Locate platelets.
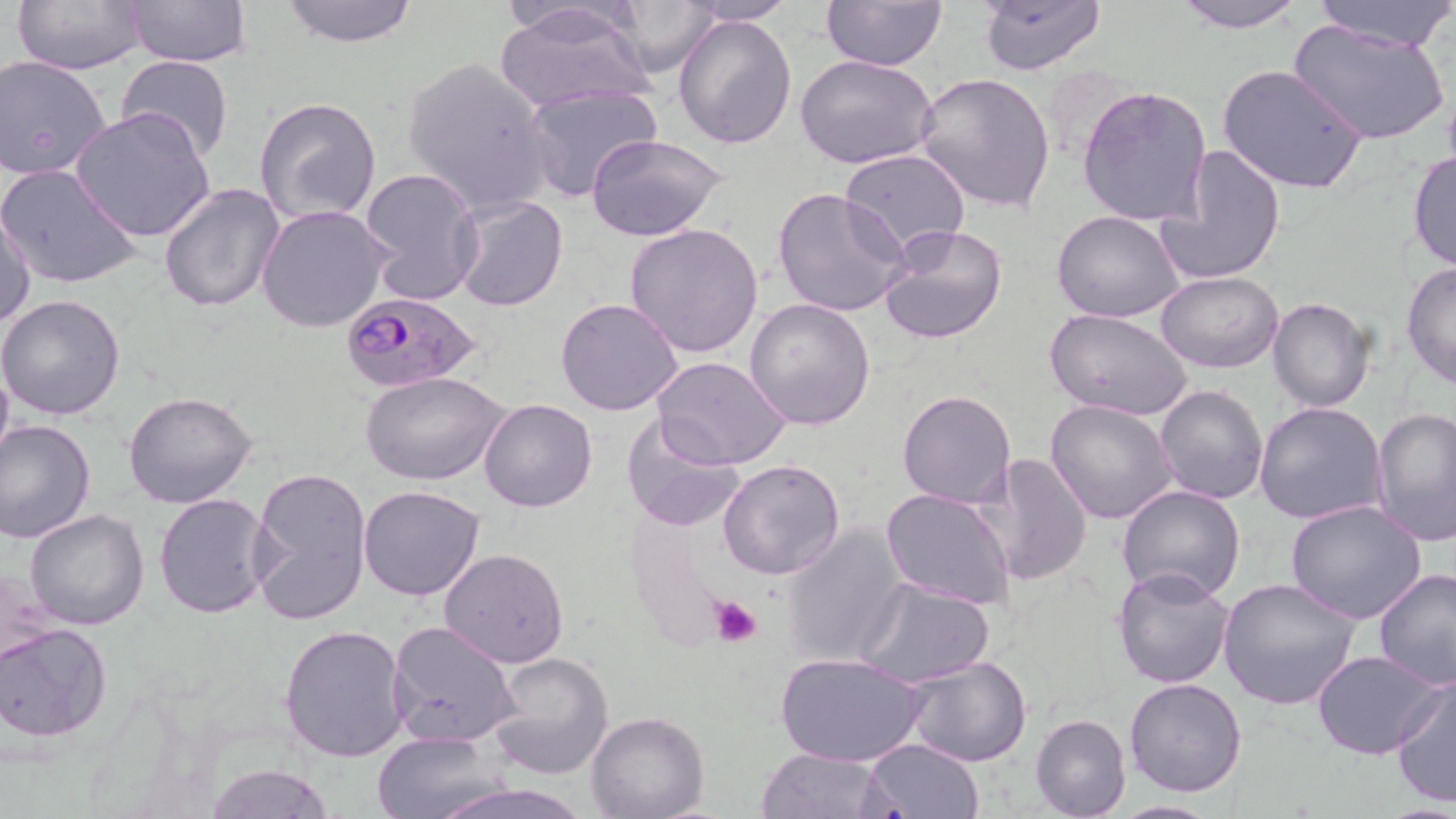
Approximate bounding boxes as (x1,y1)-(x2,y2) corner pairs in pixels.
Platelets: (708,596)-(762,646).

Uninfected red blood cell locations: (127,0)-(252,68), (276,0)-(422,47), (602,0)-(722,77), (824,0)-(947,72), (1168,0)-(1309,31), (1305,0)-(1456,51), (13,1)-(148,73), (677,1)-(798,26), (978,1)-(1106,76), (495,3)-(647,49), (495,5)-(655,114), (673,12)-(799,150), (1288,19)-(1450,147), (117,54)-(234,163), (1,55)-(111,179), (795,55)-(939,170), (401,56)-(556,214), (1217,64)-(1368,196), (914,71)-(1057,214), (519,82)-(661,203), (1077,85)-(1213,227), (255,98)-(383,227), (70,108)-(215,241), (585,132)-(730,242), (1159,144)-(1286,285), (839,148)-(971,256), (1408,151)-(1456,273), (1,162)-(141,290), (359,167)-(484,304), (158,181)-(286,313), (772,187)-(912,320), (452,194)-(568,312), (257,204)-(392,334), (1,209)-(38,327), (1051,210)-(1185,324), (624,223)-(767,359), (878,224)-(1008,345), (1401,262)-(1456,392), (1156,270)-(1283,373), (0,295)-(128,420), (744,296)-(877,431), (556,297)-(683,416), (1267,297)-(1374,412), (1045,309)-(1192,423), (0,351)-(13,471), (650,356)-(792,472), (361,371)-(511,487), (1154,383)-(1269,504), (898,390)-(1017,509), (121,391)-(260,509), (479,398)-(599,512), (1045,398)-(1179,524), (1255,400)-(1388,525), (1371,407)-(1455,545), (619,414)-(746,533), (0,420)-(96,543), (976,453)-(1093,586), (719,459)-(845,579), (247,465)-(372,630), (359,484)-(487,601), (1116,485)-(1245,604), (881,487)-(1016,610), (153,493)-(273,620), (1285,499)-(1427,624), (24,508)-(150,631), (780,522)-(909,667), (439,547)-(569,667), (1112,566)-(1236,689), (1374,569)-(1456,691), (1217,577)-(1362,710), (856,578)-(995,688), (389,621)-(521,748), (0,623)-(113,743), (279,624)-(410,762), (1312,649)-(1445,760), (488,652)-(616,779), (777,652)-(925,767), (902,655)-(1033,767), (1390,674)-(1456,810), (1124,678)-(1247,797), (585,710)-(709,819), (1030,714)-(1131,819), (372,730)-(502,819), (861,738)-(984,819), (754,747)-(894,819), (202,763)-(333,818), (418,778)-(595,819), (1108,800)-(1224,818). Plasmodium falciparum-infected red blood cell locations: (339,291)-(480,394). Slide-level diagnosis: Plasmodium falciparum. Image is 1456×819 pixels. Thin blood film. Optical microscopy. Single field of view. May-Grünwald-Giemsa stain. 1000x magnification.